Give the position of every malaria parasite and every leukocyte.
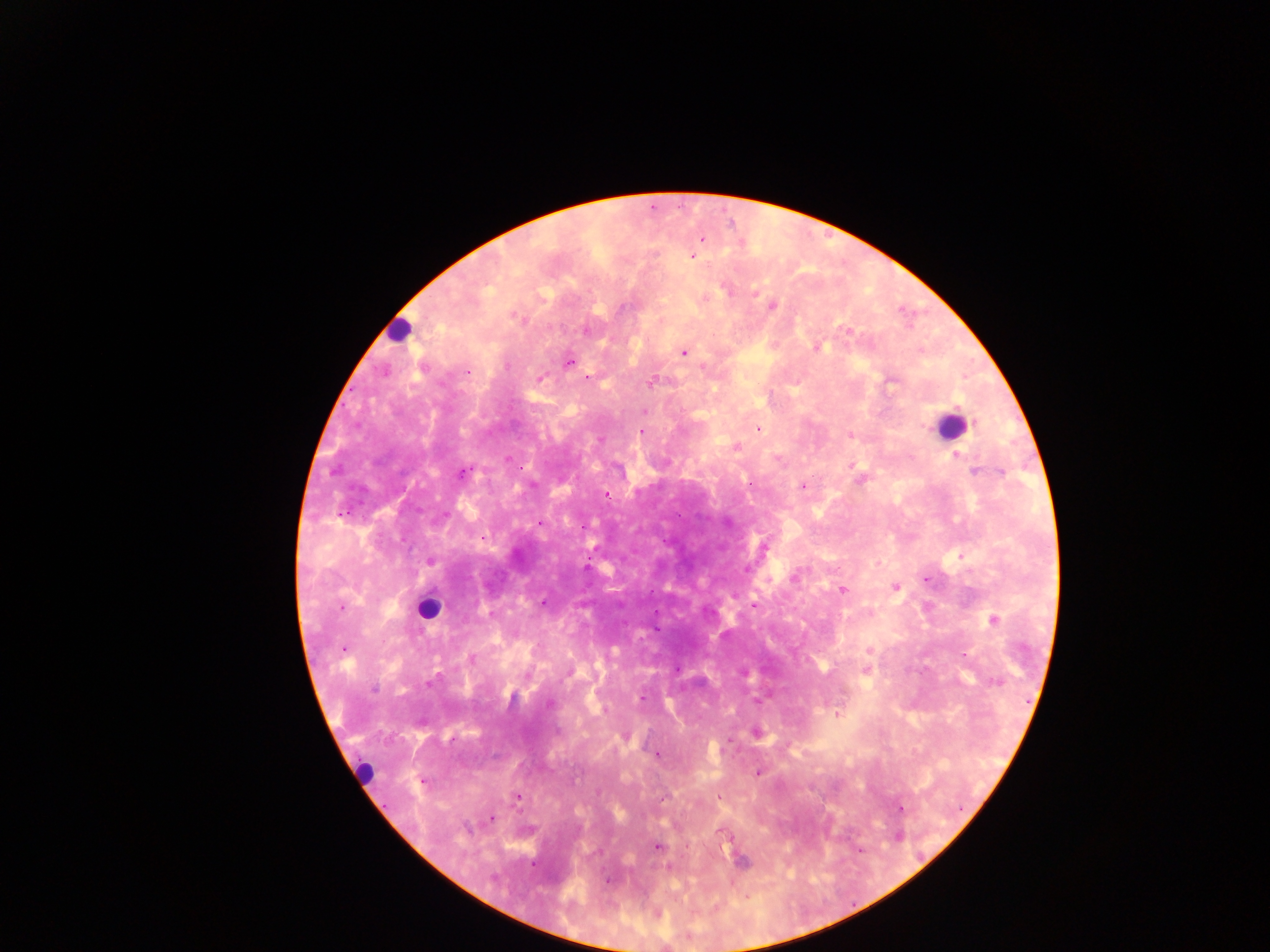

Approximate centers as {x, y} in pixels.
Malaria parasites: {700, 241}, {693, 257}, {723, 287}, {756, 294}, {706, 296}, {771, 307}, {583, 329}, {846, 330}, {818, 346}, {684, 353}, {567, 362}, {704, 367}, {468, 372}, {541, 377}, {892, 383}, {652, 384}, {645, 410}, {758, 429}, {641, 433}, {850, 434}, {600, 440}, {957, 455}, {506, 458}, {974, 471}, {462, 474}, {803, 486}, {607, 495}, {725, 522}, {431, 561}, {747, 565}, {585, 567}, {795, 576}, {895, 587}, {843, 591}, {754, 606}, {991, 619}, {345, 646}, {870, 650}, {472, 657}, {823, 666}, {869, 672}, {745, 674}, {430, 682}, {375, 689}, {844, 692}, {641, 698}, {550, 704}, {836, 715}, {756, 733}, {657, 755}, {757, 773}, {517, 796}, {718, 799}, {492, 817}, {657, 847}, {725, 848}.
Leukocytes: {399, 333}, {951, 423}, {431, 608}, {362, 773}.

One field of view. Sample from Ghana. Photographed through a microscope with a mobile-phone camera. Image is 1270×952 pixels. Thick blood film.